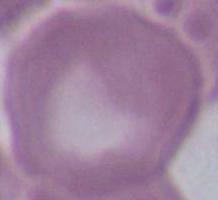
Captured at 1000x magnification. Micrograph. An erythrocyte is shown.